Report the malaria status of this cell.
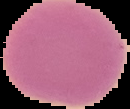

It is uninfected.

image size = 130×109 pixels
preparation = thin blood smear
image type = segmented cell region on a black background